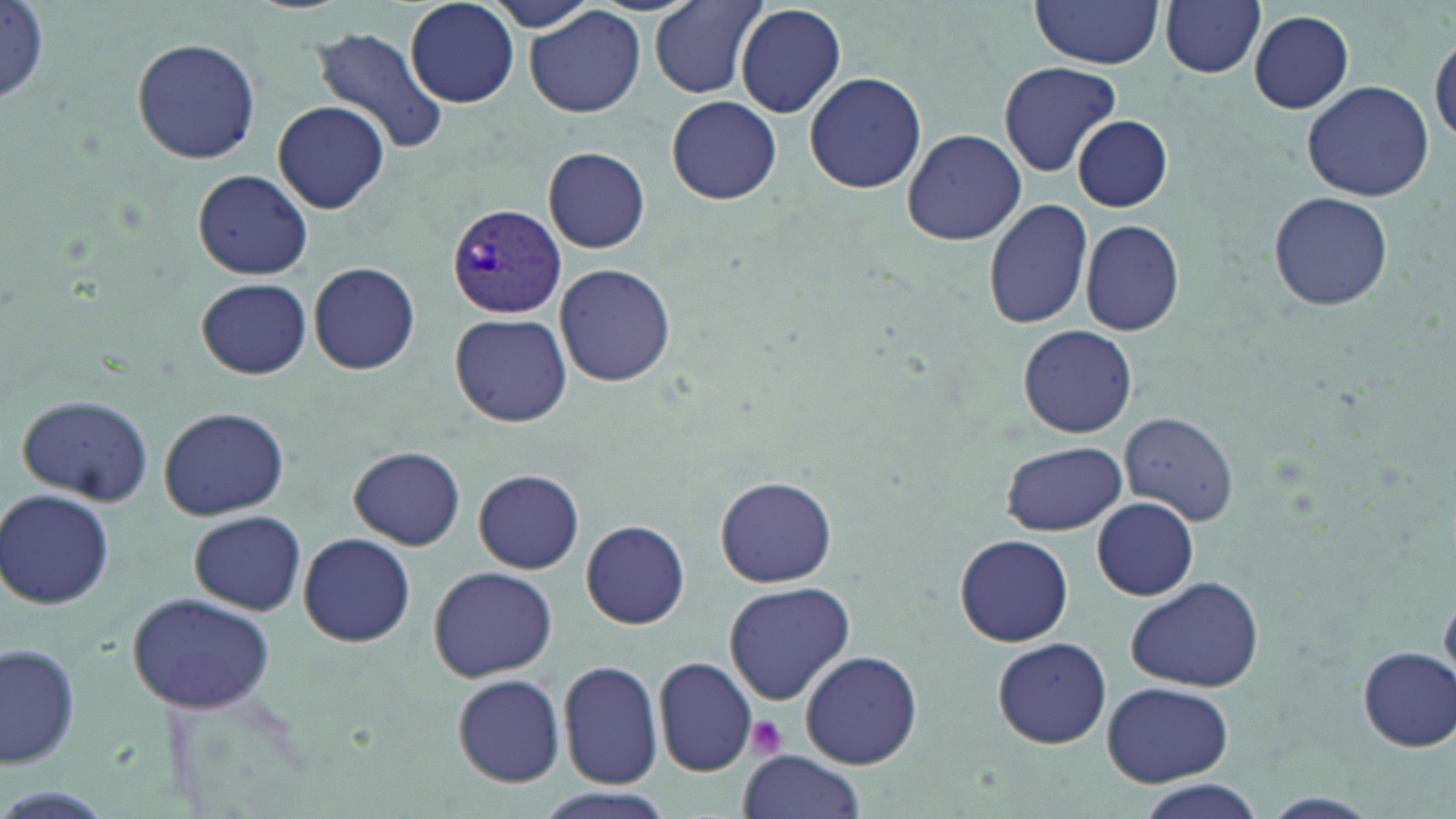
Summary:
  - Coordinate format: approximate bounding boxes as (x1,y1)-(x2,y2) corner pairs in pixels
  - Plasmodium vivax-infected red blood cell locations: (446,204)-(567,319)
  - Uninfected red blood cell locations: (405,0)-(521,108), (475,0)-(607,34), (1160,0)-(1266,79), (650,1)-(767,97), (1029,1)-(1164,68), (0,2)-(53,108), (734,4)-(845,118), (525,6)-(646,118), (1248,11)-(1354,113), (308,25)-(448,154), (1431,35)-(1456,146), (130,37)-(261,165), (997,63)-(1119,177), (804,70)-(927,195), (1302,80)-(1434,203), (666,96)-(781,205), (272,100)-(391,213), (1072,116)-(1173,212), (902,129)-(1025,245), (543,146)-(651,253), (190,168)-(314,279), (1268,191)-(1395,313), (984,198)-(1093,329), (1078,217)-(1185,336), (309,261)-(420,375), (555,263)-(674,387), (196,276)-(311,379), (450,314)-(571,427), (1019,325)-(1136,437), (14,394)-(154,507), (157,405)-(290,520), (1118,411)-(1238,525), (1001,441)-(1127,536), (350,446)-(467,549), (474,469)-(583,573), (715,476)-(836,587), (2,488)-(116,609), (1092,498)-(1199,600), (188,510)-(306,615), (581,520)-(689,629), (297,533)-(414,647), (954,534)-(1073,647), (428,565)-(557,681), (1123,574)-(1265,692), (723,581)-(855,704), (126,593)-(277,715), (990,636)-(1115,748), (0,642)-(81,770), (1358,647)-(1455,751), (798,650)-(924,768), (654,657)-(758,775), (558,659)-(663,788), (453,673)-(565,786), (1101,682)-(1234,784), (735,751)-(866,819), (1131,778)-(1269,819), (1263,792)-(1381,816)
  - Platelet locations: (745,716)-(789,762)
  - Slide-level diagnosis: Plasmodium vivax
  - Modality: optical microscopy
  - Stain: May-Grünwald-Giemsa
  - Magnification: 1000x
  - Field of view: one of a larger specimen
  - Preparation: thin blood film
  - Image size: 1456×819 pixels